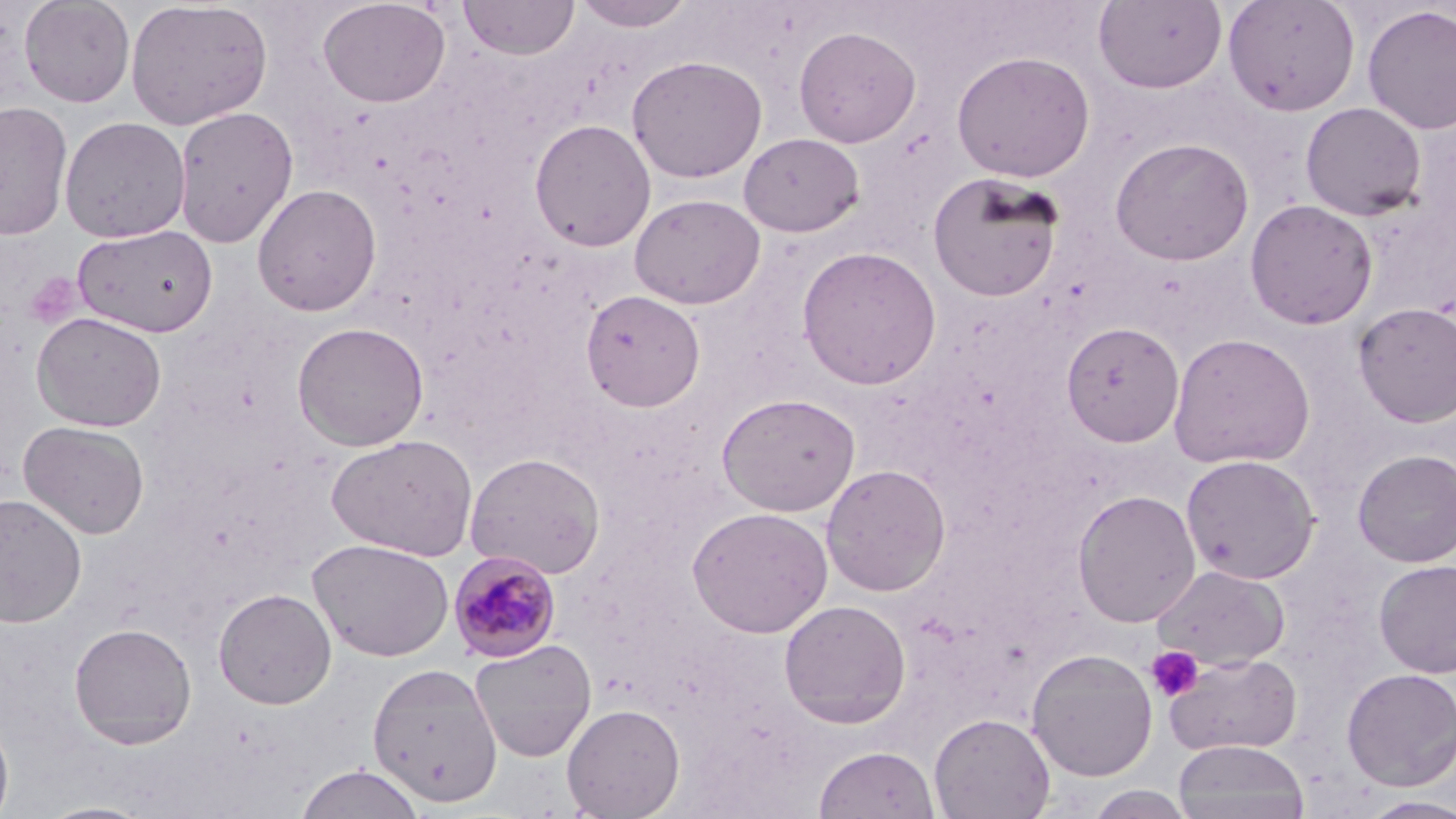

Approximate bounding boxes as named x1/y1/x2/y2 corners in pixels. Uninfected red blood cell locations (subset): (x1=19, y1=0, x2=136, y2=107), (x1=317, y1=0, x2=451, y2=108), (x1=459, y1=0, x2=579, y2=60), (x1=574, y1=0, x2=695, y2=33), (x1=1093, y1=0, x2=1228, y2=94), (x1=1222, y1=0, x2=1361, y2=116), (x1=125, y1=1, x2=274, y2=130), (x1=1362, y1=5, x2=1456, y2=135), (x1=793, y1=25, x2=921, y2=147), (x1=951, y1=50, x2=1096, y2=183), (x1=627, y1=55, x2=768, y2=182), (x1=0, y1=100, x2=73, y2=240), (x1=1299, y1=101, x2=1427, y2=221), (x1=172, y1=106, x2=298, y2=248), (x1=59, y1=116, x2=191, y2=243), (x1=529, y1=118, x2=656, y2=252), (x1=738, y1=132, x2=864, y2=238), (x1=1110, y1=137, x2=1255, y2=266), (x1=927, y1=171, x2=1065, y2=302), (x1=251, y1=183, x2=383, y2=316), (x1=628, y1=193, x2=766, y2=309), (x1=1244, y1=199, x2=1379, y2=330), (x1=72, y1=224, x2=218, y2=337), (x1=796, y1=245, x2=942, y2=389), (x1=580, y1=289, x2=706, y2=412), (x1=1353, y1=302, x2=1456, y2=428), (x1=31, y1=311, x2=167, y2=432), (x1=292, y1=321, x2=429, y2=451), (x1=1061, y1=321, x2=1185, y2=446), (x1=1168, y1=332, x2=1316, y2=469), (x1=716, y1=391, x2=861, y2=517), (x1=18, y1=420, x2=150, y2=539), (x1=326, y1=434, x2=478, y2=561), (x1=1352, y1=449, x2=1456, y2=567), (x1=465, y1=452, x2=607, y2=579), (x1=1180, y1=454, x2=1321, y2=584), (x1=821, y1=463, x2=951, y2=596), (x1=1072, y1=489, x2=1202, y2=628), (x1=0, y1=493, x2=88, y2=628), (x1=687, y1=507, x2=833, y2=638), (x1=308, y1=538, x2=454, y2=661), (x1=1373, y1=559, x2=1456, y2=679), (x1=1151, y1=563, x2=1290, y2=670), (x1=213, y1=588, x2=337, y2=710), (x1=778, y1=599, x2=912, y2=729), (x1=68, y1=622, x2=197, y2=748), (x1=468, y1=638, x2=597, y2=762), (x1=1026, y1=647, x2=1159, y2=782), (x1=1164, y1=652, x2=1302, y2=757), (x1=366, y1=662, x2=503, y2=809), (x1=1341, y1=667, x2=1456, y2=792), (x1=561, y1=703, x2=686, y2=818), (x1=0, y1=713, x2=14, y2=819), (x1=929, y1=713, x2=1055, y2=819), (x1=1172, y1=739, x2=1310, y2=819), (x1=813, y1=745, x2=940, y2=819), (x1=295, y1=763, x2=426, y2=819), (x1=1082, y1=785, x2=1197, y2=818), (x1=1359, y1=796, x2=1456, y2=818), (x1=36, y1=800, x2=158, y2=819). Platelet locations: (x1=1145, y1=646, x2=1204, y2=702). Slide-level diagnosis: Plasmodium malariae. Image is 1456×819 pixels. Optical microscopy. May-Grünwald-Giemsa-stained preparation. 1000x magnification. Thin blood smear. One field of a larger specimen.